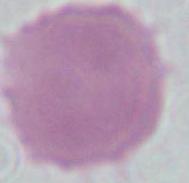
Summary:
  - Magnification: 1000x
  - Identification: erythrocyte
  - Modality: photomicrograph